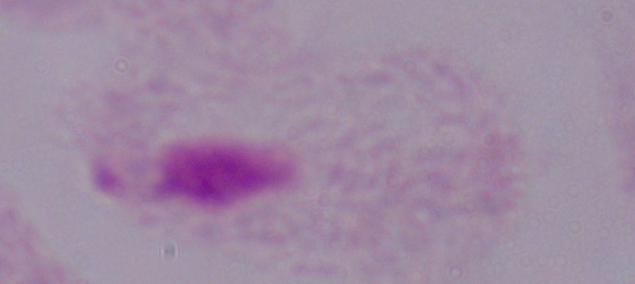
1000x magnification. Micrograph. A trichomonad is shown.